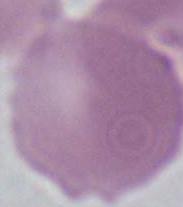
identification = erythrocyte
magnification = 1000x
modality = photomicrograph